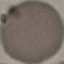

Malaria status: uninfected. Automatically extracted cell patch, resized to 64 × 64 pixels. Thin blood film. Giemsa stain. Acquired by smartphone through the microscope eyepiece.